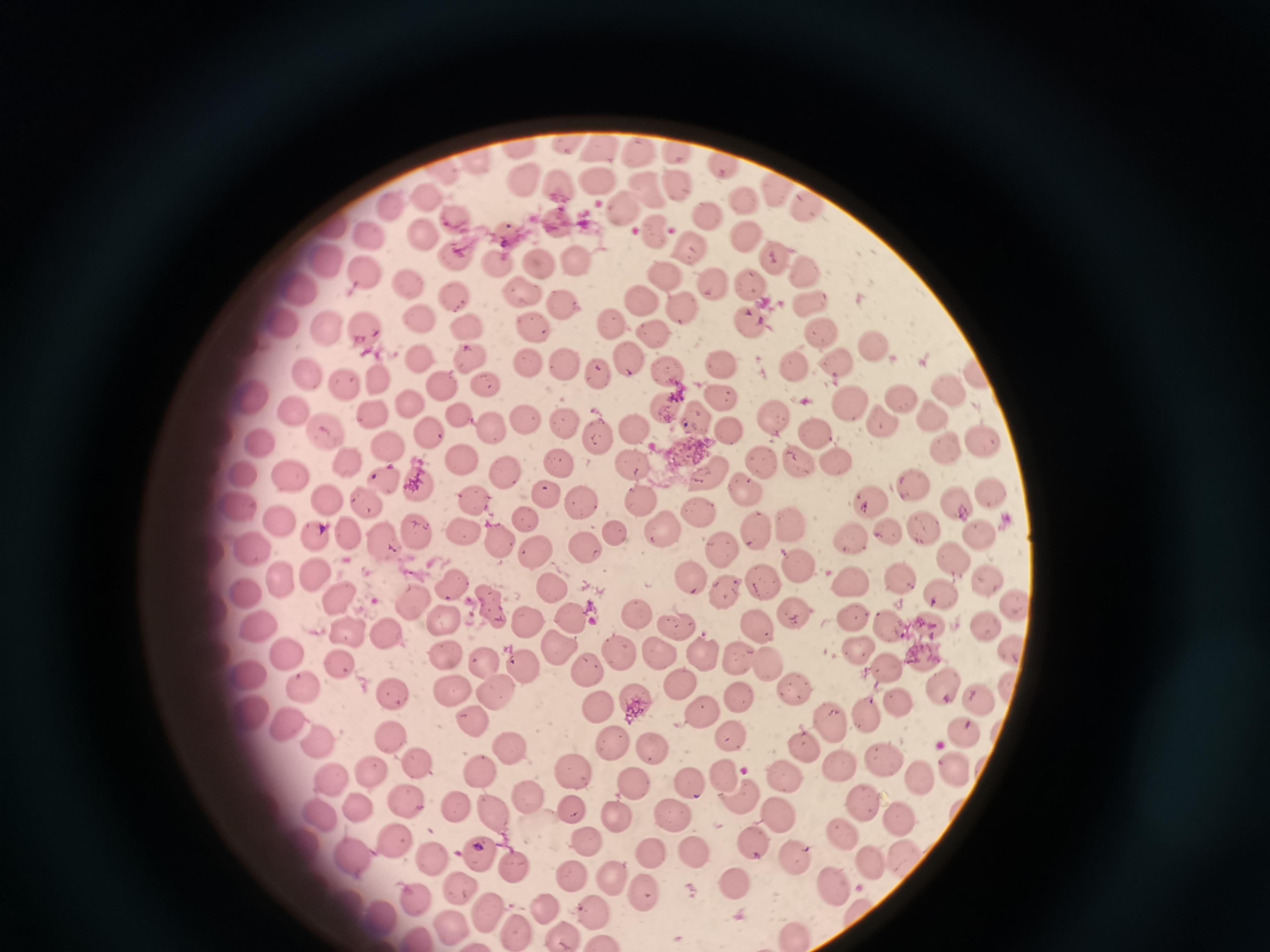
Approximate centers as [x, y] in pixels.
Summary:
  - Cell locations: [567, 142], [604, 146], [518, 147], [678, 150], [636, 155], [476, 162], [723, 167], [526, 174], [679, 181], [595, 182], [560, 183], [771, 190], [648, 192], [431, 194], [743, 198], [808, 203], [622, 206], [391, 209], [710, 214], [560, 218], [455, 223], [657, 230], [744, 234], [427, 238], [372, 239], [688, 242], [776, 258], [457, 259], [496, 260], [540, 261], [575, 261], [331, 267], [805, 270], [665, 273], [367, 276], [749, 280], [409, 281], [709, 287], [523, 288], [302, 292], [454, 295], [640, 301], [809, 301], [560, 304], [682, 309], [748, 317], [279, 319], [417, 320], [612, 321], [469, 326], [364, 328], [327, 329], [537, 330], [819, 331], [653, 333], [872, 343], [468, 356], [628, 357], [417, 358], [720, 358], [836, 362], [526, 363], [790, 363], [560, 365], [666, 370], [598, 374], [314, 375], [375, 381], [343, 383], [444, 383], [484, 384], [947, 384], [901, 394], [248, 397], [720, 399], [850, 399], [665, 404], [413, 407], [293, 413], [460, 413], [376, 414], [696, 414], [774, 415], [523, 417], [880, 417], [932, 419], [565, 425], [634, 429], [489, 430], [727, 430], [816, 430], [323, 434], [431, 435], [598, 439], [260, 442], [983, 445], [386, 447], [946, 449], [351, 458], [834, 459], [800, 460], [462, 461], [560, 462], [762, 462], [633, 463], [508, 471], [706, 473], [246, 474], [296, 476], [383, 479], [417, 482], [911, 484], [745, 488], [988, 494], [547, 495], [472, 497], [641, 497], [328, 498], [869, 498], [579, 499], [955, 499], [364, 501], [238, 508], [702, 508], [281, 518], [526, 519], [793, 519], [924, 525], [754, 527], [415, 529], [662, 530], [888, 531], [982, 532], [465, 533], [345, 535], [315, 536], [617, 536], [853, 537], [384, 539], [502, 539], [256, 547], [586, 547], [724, 548], [535, 551], [953, 558], [796, 565], [313, 574], [690, 578], [761, 578], [850, 578], [901, 578], [278, 579], [983, 579], [455, 583], [552, 587], [247, 590], [722, 590], [940, 593], [1013, 601], [339, 602], [412, 602], [490, 603], [445, 613], [640, 613], [795, 613], [566, 616], [851, 616], [530, 619], [260, 624], [675, 624], [888, 624], [931, 624], [757, 625], [984, 625], [350, 628], [386, 635], [557, 646], [856, 646], [709, 651], [445, 652], [618, 652], [1011, 652], [656, 653], [925, 654], [739, 655], [289, 656], [485, 660], [339, 664], [770, 665], [524, 666], [888, 667], [586, 671], [249, 673], [677, 678], [942, 685], [306, 686], [452, 687], [497, 690], [740, 691], [793, 691], [395, 694], [902, 698], [639, 699], [975, 699], [599, 707], [869, 708], [709, 710], [249, 718], [830, 718], [284, 722], [474, 725], [963, 728], [395, 737], [321, 740], [734, 740], [619, 744], [807, 745], [653, 747], [508, 751], [883, 759], [419, 763], [839, 766], [951, 768], [481, 769], [368, 771], [572, 771], [784, 773], [918, 775], [724, 776], [333, 778], [690, 781], [632, 785], [528, 797], [740, 797], [859, 800], [406, 803], [456, 804], [358, 808], [776, 809], [573, 811], [491, 813], [677, 813], [322, 816], [618, 817], [894, 817], [843, 833], [395, 837], [591, 840], [755, 841], [653, 851], [692, 852], [903, 854], [477, 855], [790, 855], [356, 859], [431, 859], [872, 862], [518, 870], [571, 876], [614, 877], [833, 882], [734, 884], [457, 886], [650, 890], [417, 899], [542, 905], [487, 908], [589, 910], [381, 913], [452, 927], [516, 929], [561, 933], [796, 933]
  - Capture: smartphone through the microscope eyepiece
  - Stain: Giemsa
  - Field of view: single
  - Image size: 1270×952 pixels
  - Preparation: thin blood smear